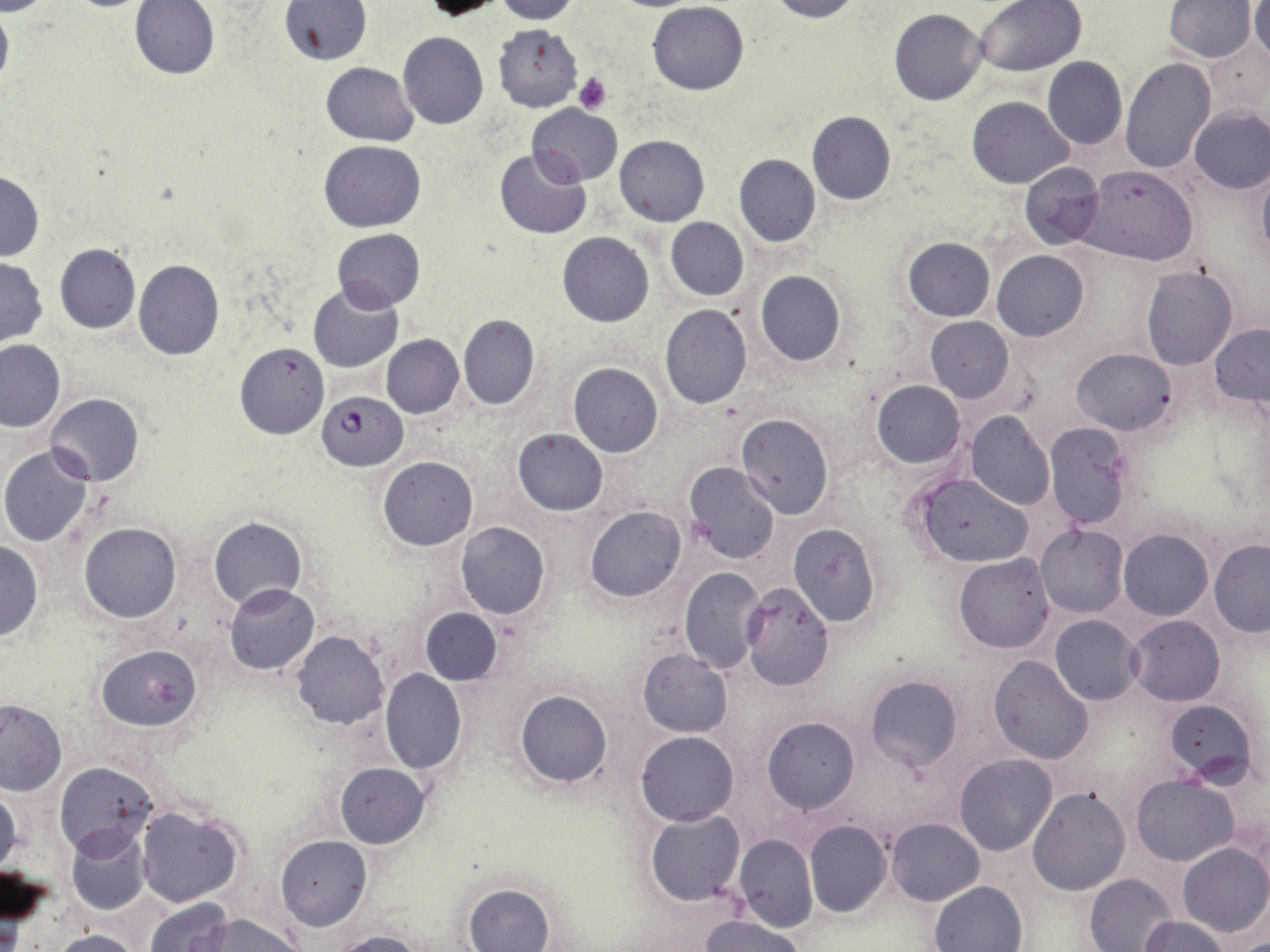

Approximate bounding boxes as [x1, y1, x2, y2] in pixels. Uninfected red blood cell locations: [130, 0, 220, 79], [420, 0, 510, 19], [491, 0, 580, 23], [767, 0, 862, 22], [977, 0, 1084, 75], [1165, 0, 1255, 62], [1248, 0, 1270, 68], [0, 1, 13, 96], [282, 1, 371, 65], [647, 2, 747, 95], [889, 9, 987, 106], [494, 23, 583, 111], [397, 32, 489, 129], [1204, 38, 1270, 122], [1042, 56, 1126, 149], [1121, 59, 1215, 173], [320, 61, 418, 146], [966, 96, 1073, 188], [528, 103, 622, 186], [1189, 106, 1270, 193], [807, 111, 895, 205], [615, 134, 708, 226], [320, 140, 425, 232], [495, 147, 591, 239], [734, 154, 821, 247], [1020, 162, 1104, 249], [1081, 165, 1197, 264], [1257, 166, 1270, 263], [0, 170, 44, 260], [666, 217, 748, 301], [333, 228, 424, 309], [558, 232, 653, 327], [902, 238, 995, 322], [55, 243, 140, 334], [992, 250, 1088, 341], [0, 257, 47, 345], [133, 260, 224, 360], [1142, 266, 1238, 369], [755, 270, 844, 367], [309, 282, 402, 373], [660, 304, 751, 408], [458, 314, 539, 410], [924, 317, 1014, 403], [1210, 323, 1270, 410], [382, 335, 464, 418], [0, 339, 65, 431], [234, 342, 330, 440], [1073, 348, 1175, 435], [568, 364, 663, 457], [872, 380, 965, 468], [45, 394, 144, 486], [966, 412, 1054, 510], [735, 414, 833, 520], [1044, 422, 1133, 529], [691, 428, 820, 550], [512, 429, 608, 514], [1, 445, 95, 546], [377, 457, 477, 550], [683, 462, 780, 564], [914, 473, 1034, 567], [584, 506, 686, 602], [210, 516, 306, 611], [456, 522, 550, 619], [80, 523, 180, 623], [788, 523, 880, 626], [1036, 524, 1129, 616], [1119, 529, 1212, 621], [0, 541, 43, 641], [1209, 541, 1270, 636], [953, 552, 1056, 653], [679, 568, 766, 673], [741, 583, 835, 691], [224, 584, 320, 674], [421, 608, 501, 684], [1051, 615, 1143, 705], [1126, 616, 1224, 706], [291, 631, 389, 729], [96, 643, 201, 731], [638, 649, 733, 737], [989, 656, 1094, 762], [381, 668, 466, 773], [863, 673, 963, 775], [515, 691, 611, 787], [1165, 699, 1257, 785], [0, 700, 66, 796], [762, 717, 858, 812], [636, 730, 738, 825], [955, 754, 1057, 855], [55, 762, 157, 858], [334, 762, 430, 848], [1133, 775, 1237, 865], [0, 787, 22, 878], [1027, 787, 1130, 895], [135, 806, 245, 907], [645, 811, 744, 905], [885, 817, 983, 905], [804, 821, 891, 917], [66, 824, 152, 915], [277, 834, 370, 930], [734, 835, 816, 933], [1178, 842, 1270, 937], [1085, 873, 1178, 952], [930, 881, 1027, 951], [463, 882, 556, 952], [145, 898, 231, 952], [193, 914, 302, 952], [700, 914, 806, 952], [1138, 915, 1232, 951], [52, 930, 142, 952], [333, 930, 429, 952]. Platelet locations: [573, 72, 611, 113]. Plasmodium falciparum-infected red blood cell locations: [317, 390, 406, 472]. Slide-level diagnosis: Plasmodium falciparum. Image is 1270×952 pixels. Single field of view. Optical microscopy. May-Grünwald-Giemsa stain. Thin blood film. 1000x magnification.